State which parasite is depicted.
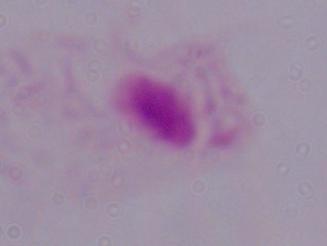
This is a trichomonad.

modality: photomicrograph
magnification: 1000x